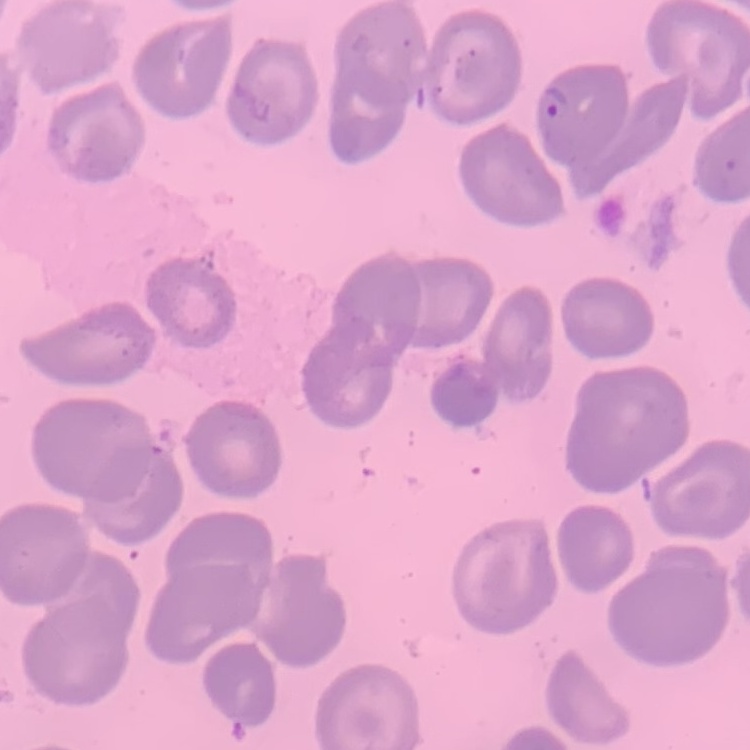
{
  "red_blood_cell_morphology": "no rouleaux formation",
  "stain": "Field's or Giemsa",
  "preparation": "thin blood film",
  "image_type": "one tile cut from a larger photomicrograph"
}